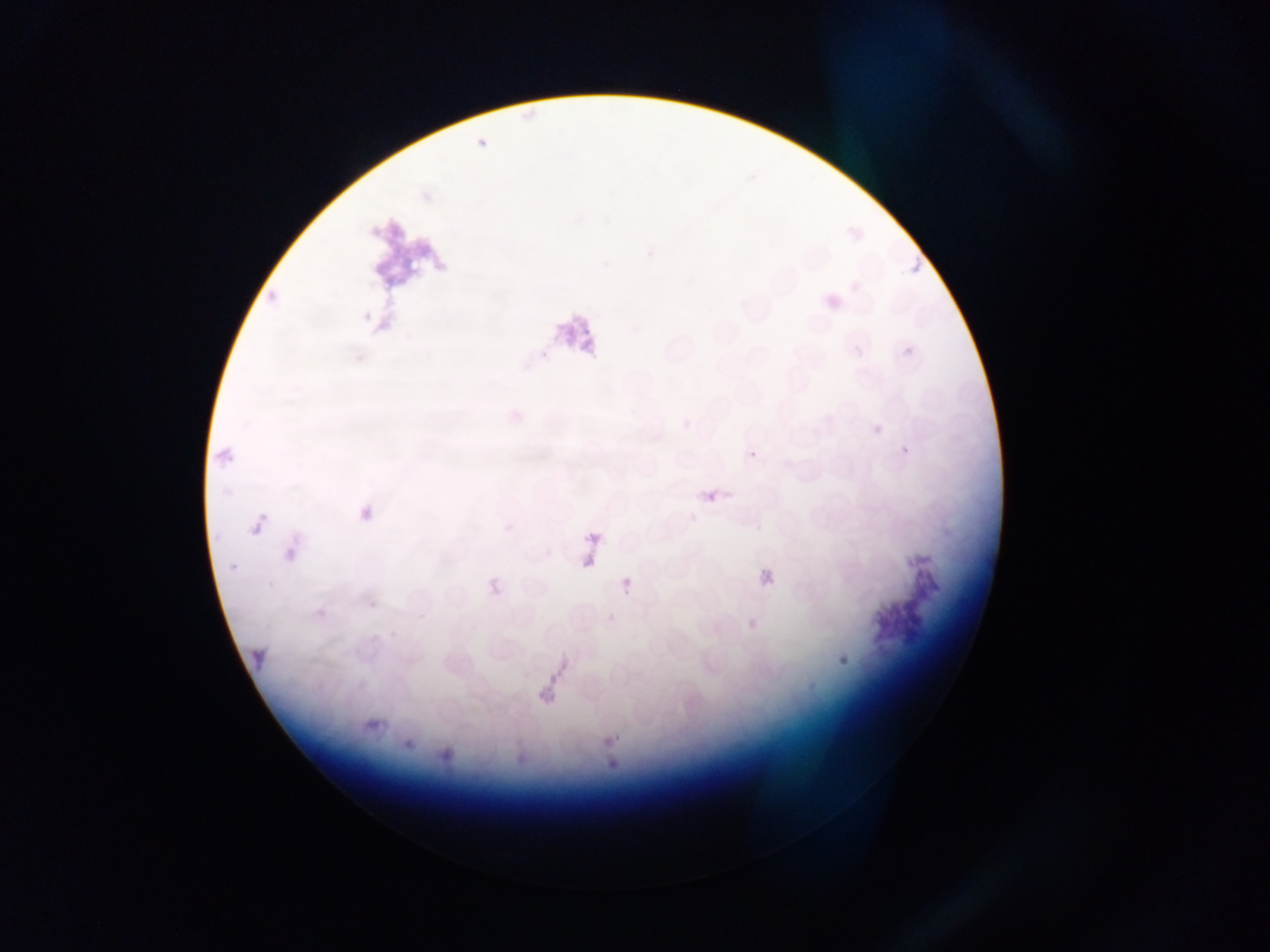

Approximate bounding boxes as (left, top, right, bottom) in pixels.
Summary:
  - Artifact (stain precipitate or debris) locations: (362, 205, 462, 306), (541, 298, 620, 389), (569, 519, 605, 565), (855, 529, 943, 645), (238, 630, 271, 671), (516, 646, 594, 709)
  - Malaria parasite locations: (903, 249, 931, 282), (749, 449, 759, 460), (706, 489, 721, 503), (355, 502, 380, 528), (247, 513, 272, 540), (281, 547, 299, 566), (758, 567, 777, 587), (619, 576, 635, 594)
  - Field of view: single
  - Capture: mobile-phone photograph through a microscope
  - Preparation: thin blood smear
  - Image size: 1270×952 pixels
  - Country: Ghana